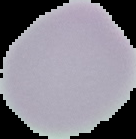

malaria status = uninfected
preparation = thin blood smear
image type = cell region segmented out of the field of view; surrounding area masked to black
image size = 136×139 pixels